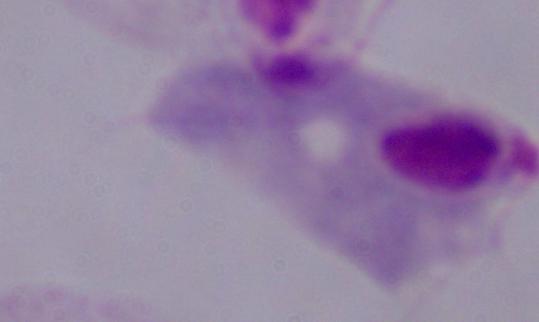

Summary:
  - Modality: micrograph
  - Magnification: 1000x
  - Identification: trichomonad